Report the malaria status of this cell.
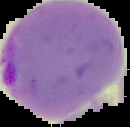

It is parasitized.

image type = cell region segmented out of the field of view; surrounding area masked to black
image size = 130×127 pixels
preparation = thin blood film